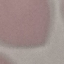
Summary:
  - Result: no malaria parasites detected
  - Capture: smartphone through the microscope eyepiece
  - Stain: Giemsa
  - Preparation: thin smear
  - Image type: automatically extracted cell patch, resized to 64 × 64 pixels